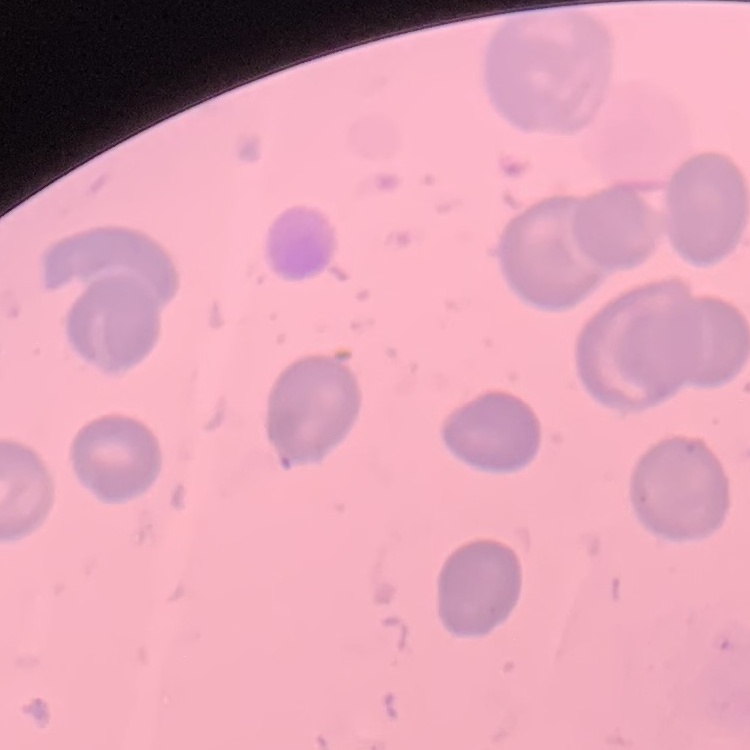

red blood cell morphology = no rouleaux formation
preparation = thin blood film
stain = Field's or Giemsa
image type = square crop of a larger photomicrograph